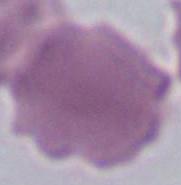

Micrograph. A red blood cell is shown. 1000x magnification.